Outline each Plasmodium falciparum parasite and classify it by life-cycle stage.
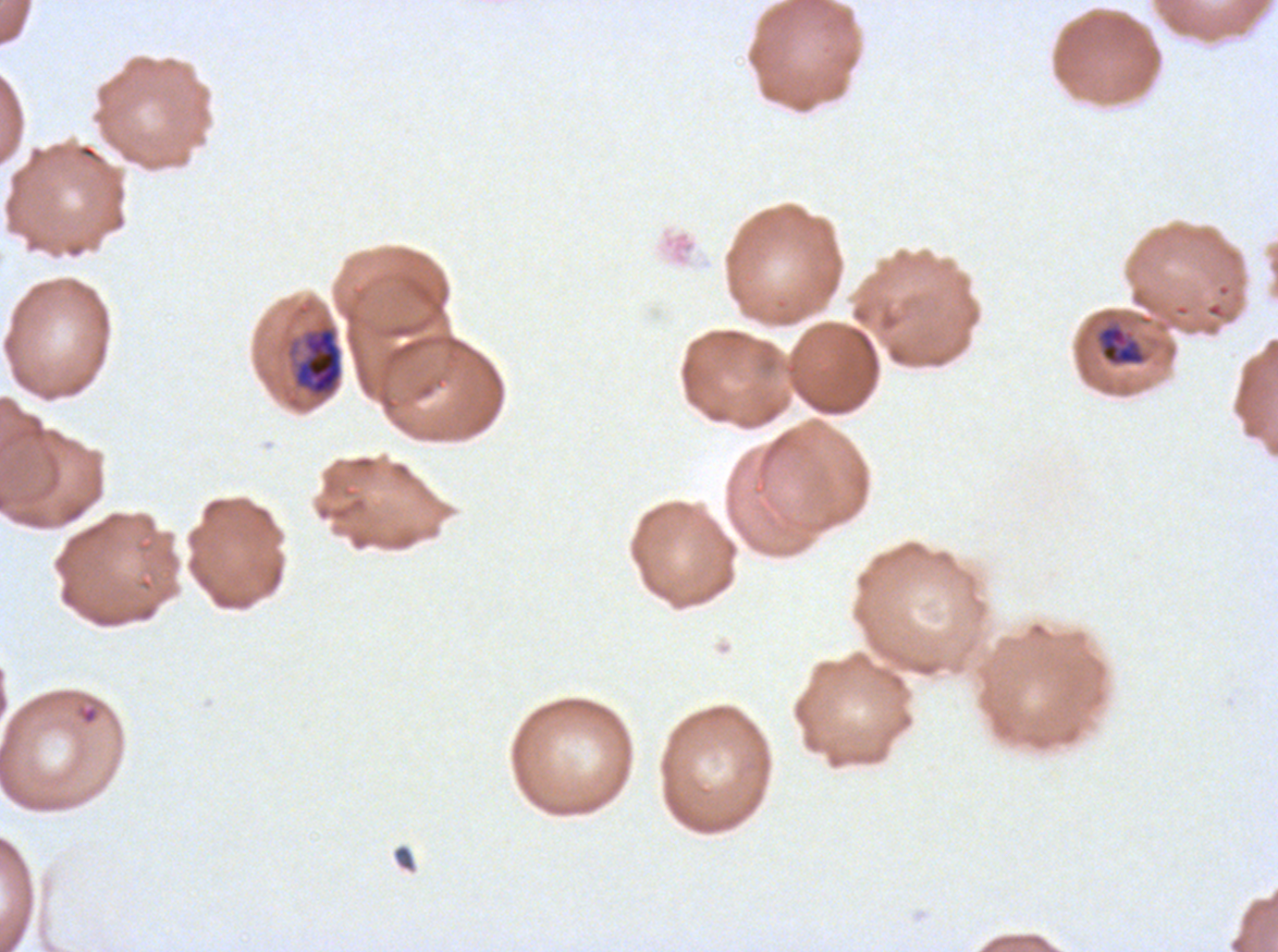

Approximate bounding boxes as (x1, y1, x2, y2) in pixels.
Rings: (75, 702, 101, 726).
Late trophozoites: (1095, 323, 1148, 367).
Early schizonts: (285, 322, 344, 400).
No late-ring/early-trophozoite forms, mid trophozoites, late schizonts, segmenters, or gametocytes observed.

Ex-vivo Plasmodium falciparum culture from a patient in The Gambia, grown for 24 to 48 hours. One sub-image of a larger composite. Giemsa-stained preparation. Life-cycle stages observed: ring, late trophozoite, early schizont. Thin blood film. Image is 1278×952 pixels.